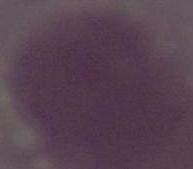

Captured at 1000x magnification. A red blood cell is seen. Micrograph.